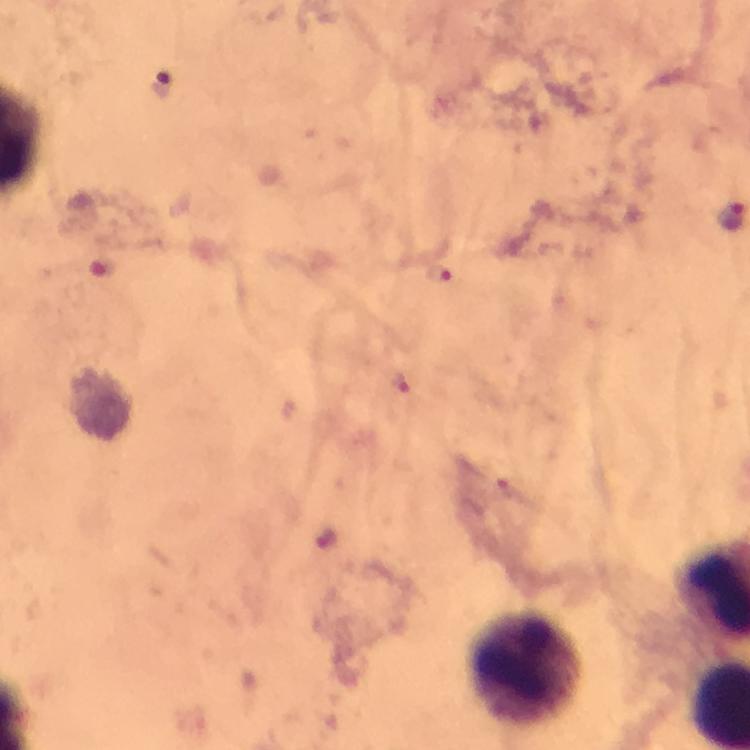 Approximate centers as {x, y} in pixels. Leukocyte locations: {527, 671}. Plasmodium parasite locations: {103, 266}, {440, 274}. Image is 750×750 pixels. Thick blood film. Cropped region of a single field of view. Photographed with a smartphone mounted on the microscope. At 100x magnification. From a diagnostic examination for malaria. Immersion oil was used. Giemsa stain.